Assess this cell for malaria.
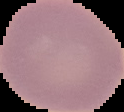

Uninfected.

image size = 124×112 pixels
image type = segmented cell region on a black background
preparation = thin blood film